Locate every Plasmodium malariae-infected red blood cell.
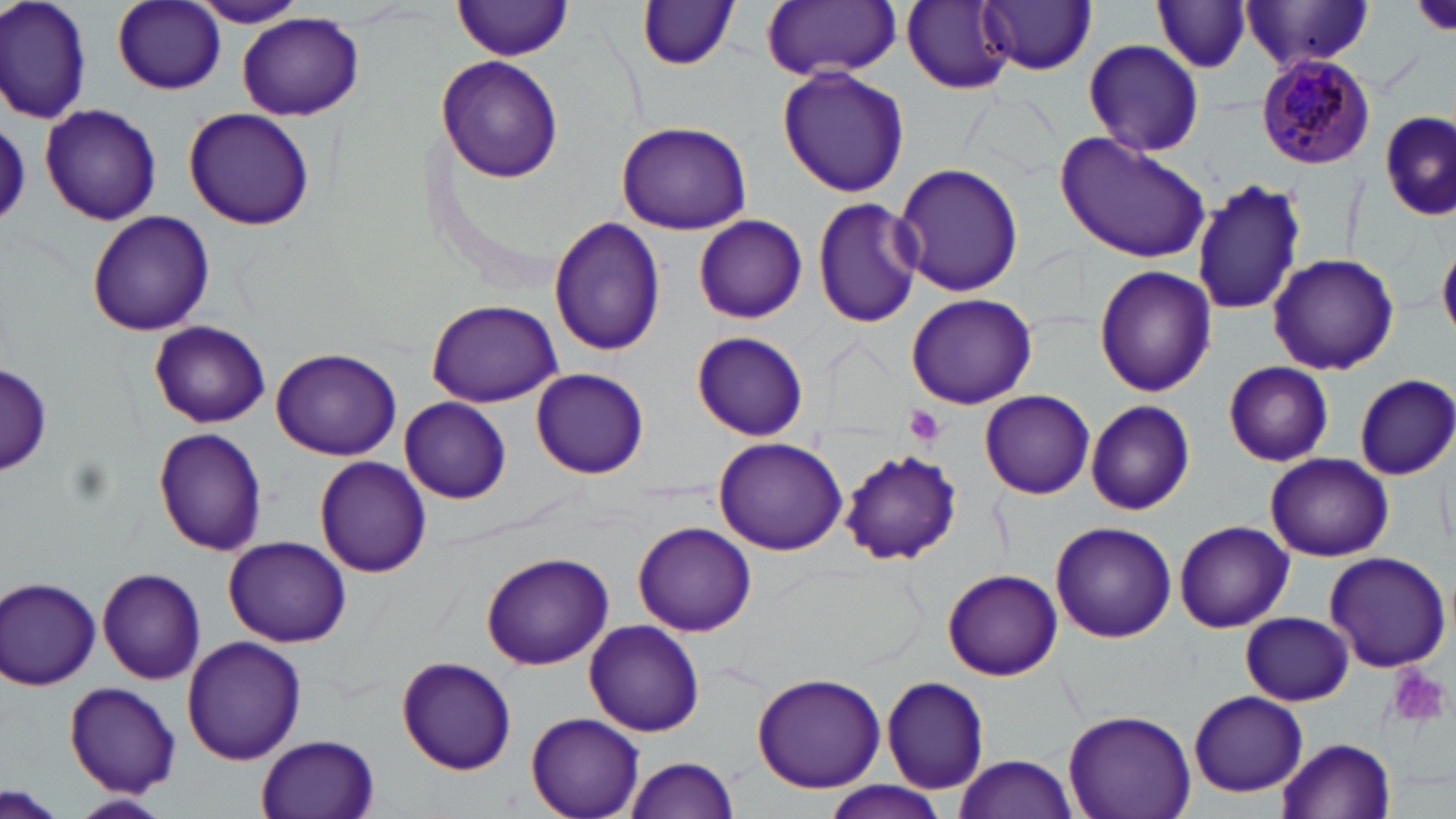

Approximate bounding boxes as (x1, y1, x2, y2) in pixels.
Plasmodium malariae-infected red blood cells: (1254, 53, 1377, 171).

Summary:
  - Uninfected red blood cell locations: (0, 0, 91, 122), (761, 0, 901, 81), (902, 0, 1015, 91), (979, 0, 1097, 75), (113, 1, 225, 94), (188, 1, 309, 27), (1238, 1, 1378, 73), (453, 2, 574, 60), (638, 2, 740, 70), (1152, 3, 1253, 74), (237, 13, 367, 122), (1082, 39, 1204, 157), (437, 55, 563, 182), (778, 66, 910, 197), (38, 104, 159, 225), (184, 106, 314, 230), (1378, 112, 1454, 221), (0, 120, 28, 227), (615, 122, 754, 235), (1055, 135, 1212, 264), (893, 162, 1024, 297), (1191, 177, 1308, 318), (812, 197, 922, 328), (86, 210, 216, 337), (549, 215, 666, 358), (694, 215, 807, 322), (1438, 239, 1456, 339), (1267, 252, 1400, 375), (1095, 265, 1215, 397), (905, 292, 1039, 409), (425, 297, 563, 408), (149, 320, 270, 429), (691, 331, 809, 440), (269, 347, 401, 459), (0, 360, 51, 482), (1223, 361, 1334, 467), (531, 368, 650, 479), (1354, 374, 1456, 480), (980, 391, 1095, 500), (400, 397, 511, 504), (1085, 400, 1194, 513), (154, 428, 266, 556), (710, 437, 847, 554), (839, 448, 961, 566), (1266, 453, 1392, 560), (313, 456, 432, 577), (1175, 520, 1293, 632), (634, 523, 756, 637), (1052, 523, 1176, 644), (221, 537, 353, 647), (481, 552, 614, 670), (1323, 552, 1452, 673), (97, 567, 206, 684), (942, 570, 1062, 681), (2, 576, 102, 691), (1241, 611, 1354, 705), (585, 619, 707, 737), (181, 635, 305, 764), (396, 654, 516, 775), (752, 672, 885, 792), (880, 676, 990, 795), (65, 683, 182, 797), (1188, 691, 1308, 798), (1063, 710, 1195, 819), (526, 713, 645, 819), (258, 733, 380, 818), (1280, 736, 1398, 819), (953, 754, 1077, 819), (624, 756, 741, 818), (0, 784, 62, 819), (823, 784, 949, 819), (66, 793, 173, 819)
  - Platelet locations: (1414, 0, 1455, 37), (905, 405, 945, 446), (1388, 666, 1450, 727)
  - Slide-level diagnosis: Plasmodium malariae
  - Stain: May-Grünwald-Giemsa
  - Image size: 1456×819 pixels
  - Modality: light microscopy
  - Magnification: 1000x
  - Preparation: thin blood film
  - Field of view: single